Locate every leukocyte (white blood cell).
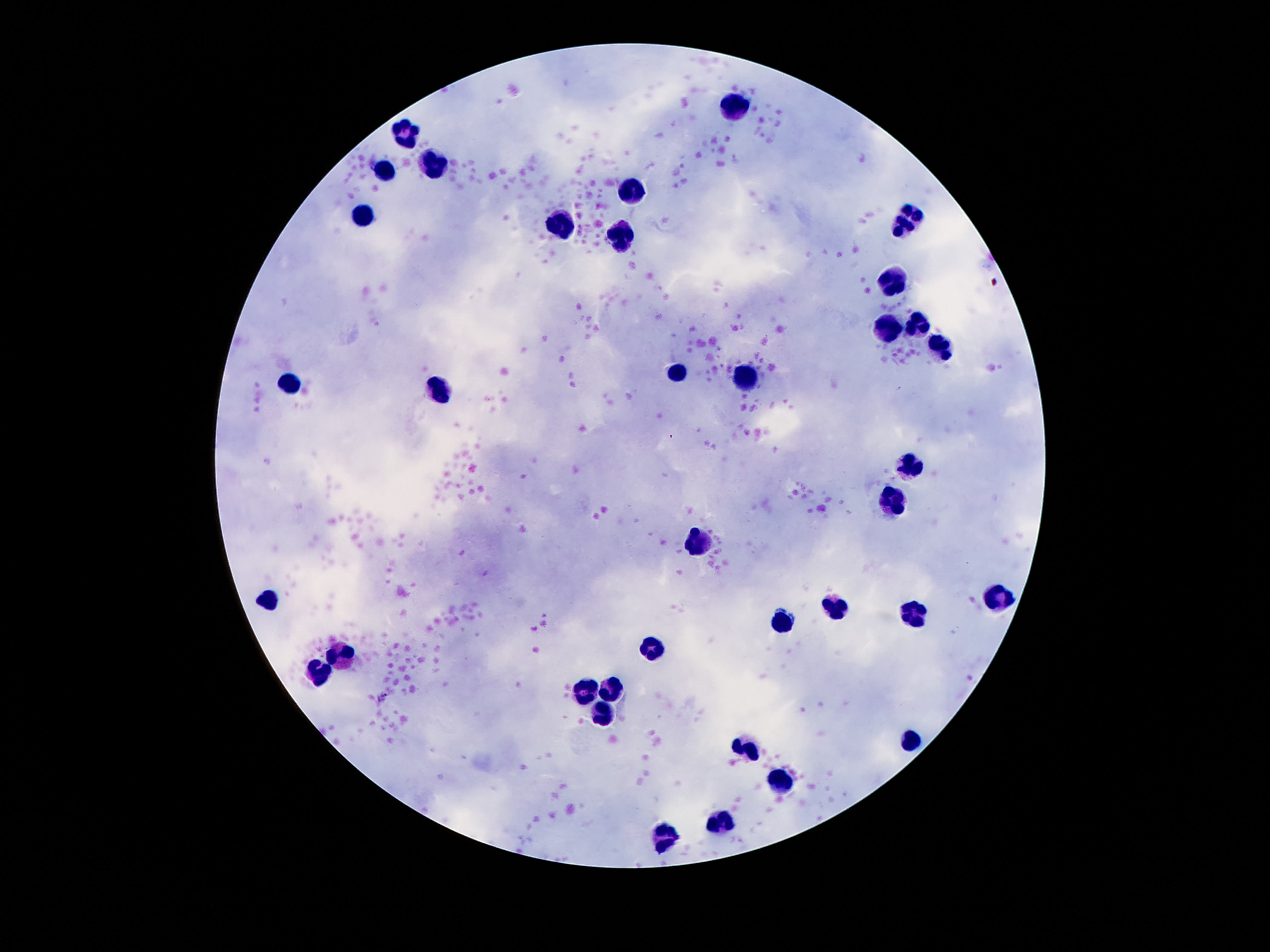

Approximate object centers, in pixels from the top-left corner.
Leukocytes: (x=735, y=105), (x=405, y=134), (x=434, y=163), (x=385, y=171), (x=635, y=190), (x=366, y=216), (x=913, y=225), (x=557, y=229), (x=622, y=237), (x=899, y=282), (x=920, y=324), (x=889, y=327), (x=940, y=354), (x=678, y=370), (x=751, y=378), (x=292, y=382), (x=440, y=388), (x=907, y=464), (x=895, y=499), (x=694, y=539), (x=1002, y=598), (x=272, y=602), (x=836, y=604), (x=913, y=615), (x=784, y=623), (x=649, y=646), (x=344, y=656), (x=317, y=673), (x=610, y=687), (x=583, y=689), (x=600, y=709), (x=909, y=738), (x=747, y=748), (x=782, y=783), (x=721, y=821), (x=665, y=836).

magnification: 100x
field_of_view: single
capture: smartphone camera through the microscope eyepiece
preparation: thick blood smear
patient_malaria_status: negative
image_size: 1270×952 pixels
stain: Giemsa